Describe the morphology of the erythrocytes.
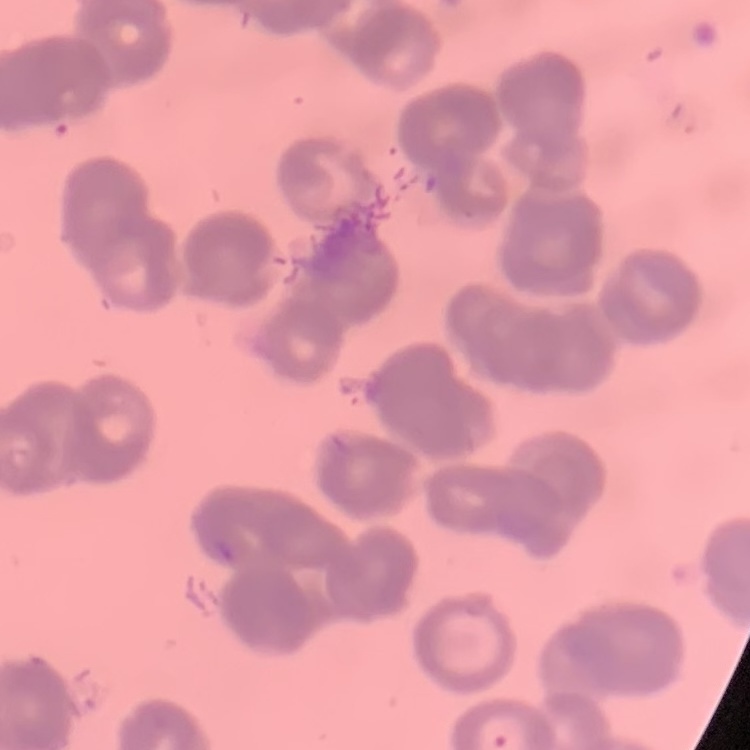

They show rouleaux formation.

Summary:
  - Preparation: thin blood film
  - Stain: Field's or Giemsa
  - Image type: square crop of a larger photomicrograph